Classify this cell by malaria status.
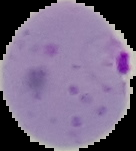

It is parasitized.

From a thin blood film. The area outside the segmented cell region is set to black. Image is 136×151 pixels.